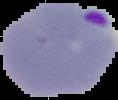

malaria status = parasitized
preparation = thin blood smear
image type = segmented cell region with the area outside set to black
image size = 118×100 pixels